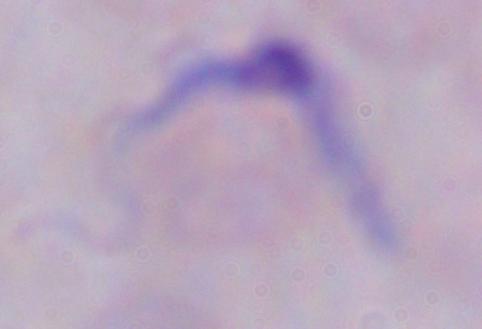

modality: micrograph
magnification: 1000x
identification: trypanosome